Outline platelets.
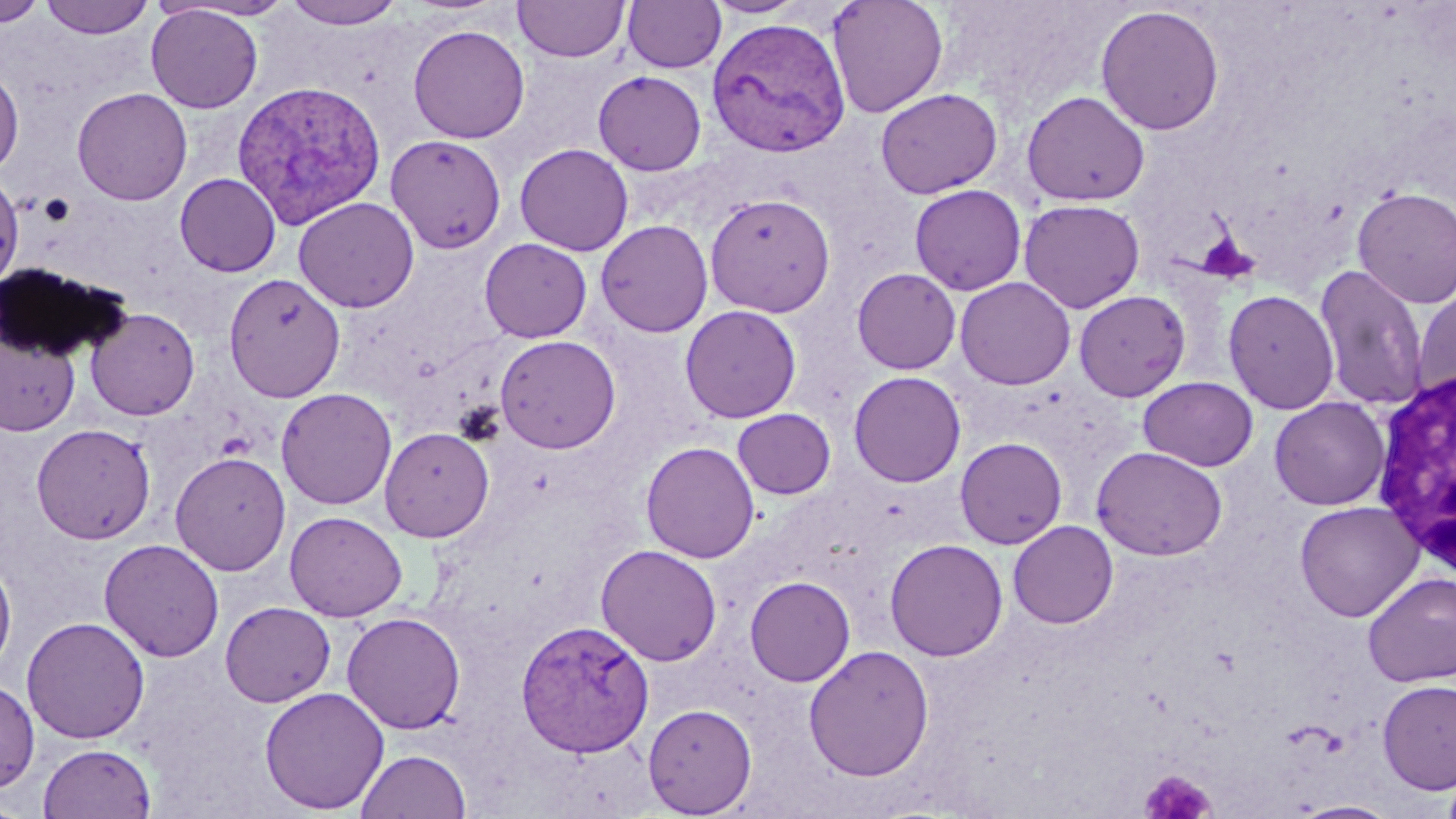

Approximate bounding boxes as (x1, y1, x2, y2) in pixels.
Platelets: (1194, 231, 1255, 282), (1139, 768, 1216, 817).

Summary:
  - White blood cell locations: (1369, 366, 1456, 578)
  - Uninfected red blood cell locations: (1, 0, 45, 26), (39, 0, 155, 39), (282, 0, 406, 28), (513, 0, 629, 62), (704, 0, 810, 19), (827, 0, 948, 118), (622, 1, 726, 73), (146, 4, 263, 113), (1095, 4, 1225, 135), (408, 24, 530, 143), (0, 66, 24, 175), (593, 70, 707, 175), (72, 87, 192, 206), (875, 87, 1003, 199), (1021, 90, 1150, 207), (385, 134, 507, 254), (515, 143, 634, 255), (0, 172, 24, 290), (175, 173, 281, 276), (909, 184, 1027, 295), (1351, 187, 1456, 308), (703, 192, 835, 317), (294, 197, 419, 313), (1018, 199, 1145, 313), (595, 219, 713, 338), (479, 238, 593, 342), (1314, 265, 1430, 411), (852, 268, 961, 374), (224, 273, 345, 401), (955, 277, 1075, 390), (1412, 287, 1456, 407), (1223, 289, 1339, 415), (1074, 290, 1191, 401), (679, 305, 802, 423), (85, 307, 200, 420), (0, 330, 79, 436), (495, 335, 621, 453), (848, 371, 966, 487), (1138, 377, 1258, 471), (276, 387, 397, 509), (1269, 397, 1390, 510), (732, 408, 836, 499), (31, 423, 156, 545), (379, 427, 494, 541), (954, 437, 1068, 549), (640, 441, 760, 563), (1091, 446, 1228, 560), (170, 452, 291, 576), (1295, 501, 1423, 622), (284, 511, 407, 622), (1008, 520, 1118, 629), (885, 538, 1008, 661), (98, 539, 224, 662), (595, 544, 722, 666), (0, 557, 17, 678), (1362, 572, 1456, 686), (745, 576, 855, 687), (220, 601, 336, 707), (341, 611, 467, 734), (22, 616, 150, 744), (803, 644, 934, 781), (0, 678, 39, 793), (1377, 680, 1456, 794), (259, 686, 390, 814), (643, 703, 757, 817), (38, 743, 156, 818), (356, 748, 472, 819), (1441, 767, 1456, 819), (0, 796, 30, 819), (1287, 800, 1401, 818)
  - Plasmodium vivax-infected red blood cell locations: (707, 16, 851, 158), (232, 79, 387, 228), (517, 619, 655, 757)
  - Slide-level diagnosis: Plasmodium vivax
  - Preparation: thin blood film
  - Field of view: one of a larger specimen
  - Modality: light microscopy
  - Image size: 1456×819 pixels
  - Stain: May-Grünwald-Giemsa
  - Magnification: 1000x